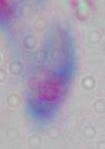

modality: photomicrograph
identification: Toxoplasma gondii
magnification: 1000x